Name the parasite shown.
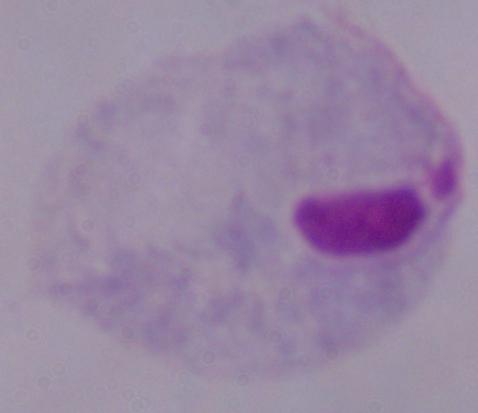
This is a trichomonad.

{
  "magnification": "1000x",
  "modality": "micrograph"
}